Name the cell type shown.
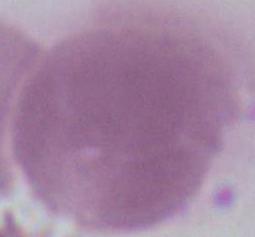
An erythrocyte.

1000x magnification. Photomicrograph.